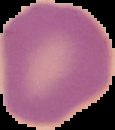 Image is 115×130 pixels. The area outside the segmented cell region is set to black. Result: no malaria parasites detected. From a thin blood smear.